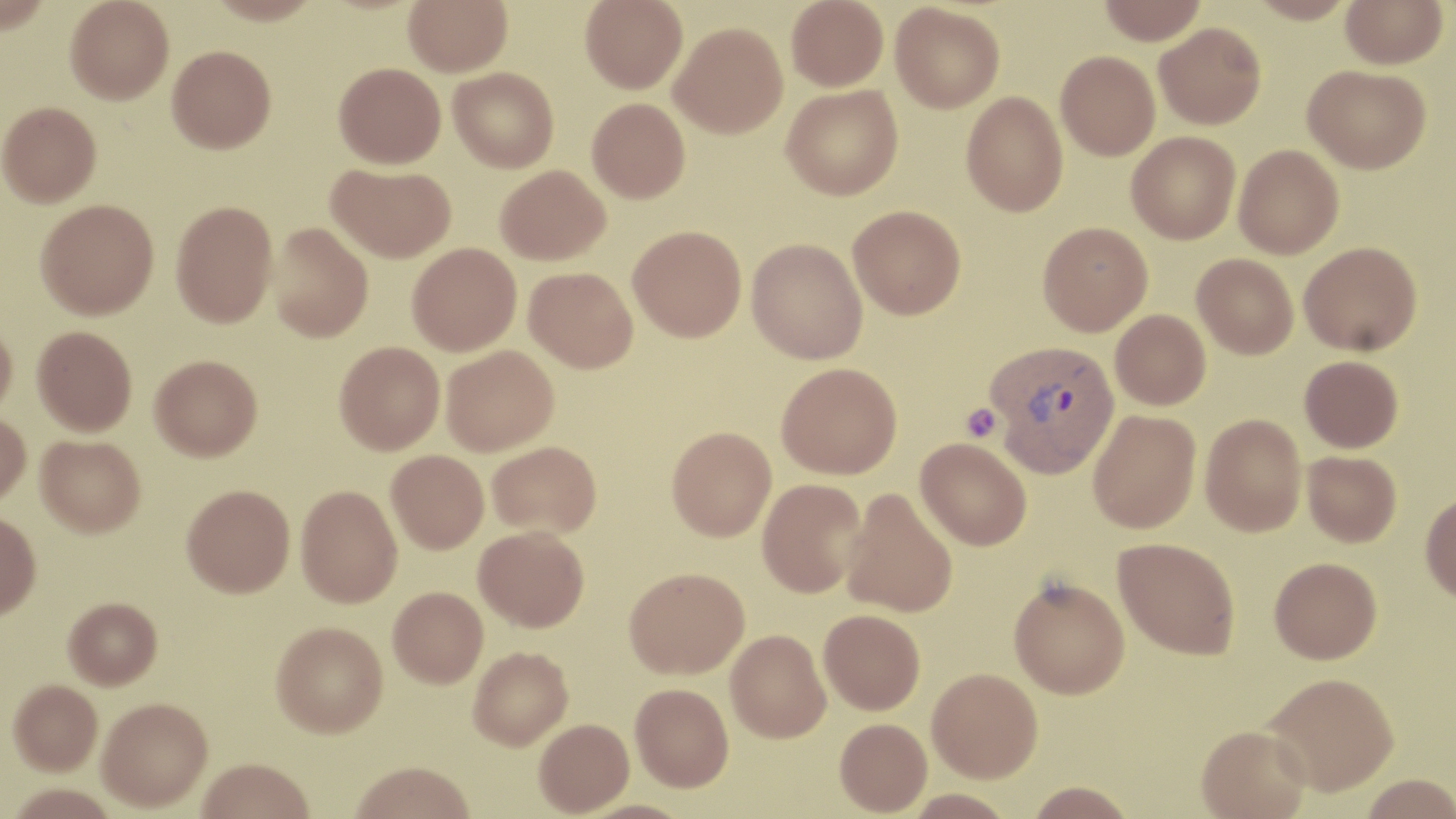
Summary:
  - Coordinate format: approximate bounding boxes as (x1, y1, x2, y2) in pixels
  - Uninfected red blood cell locations: (0, 0, 52, 34), (65, 0, 174, 104), (204, 0, 325, 25), (404, 0, 512, 76), (580, 0, 687, 93), (786, 0, 889, 90), (1096, 0, 1208, 43), (1245, 0, 1360, 23), (1341, 0, 1448, 68), (890, 3, 1005, 113), (669, 21, 788, 138), (1154, 22, 1266, 129), (167, 45, 276, 153), (1056, 51, 1160, 160), (333, 62, 446, 169), (1303, 64, 1431, 173), (449, 67, 558, 173), (781, 85, 902, 200), (961, 91, 1068, 217), (587, 98, 690, 203), (0, 101, 102, 207), (1127, 131, 1241, 244), (1233, 144, 1343, 258), (326, 162, 456, 262), (496, 165, 610, 265), (36, 198, 159, 319), (171, 200, 278, 327), (848, 204, 966, 319), (268, 222, 373, 342), (1037, 222, 1153, 335), (627, 225, 746, 341), (747, 238, 868, 364), (1299, 241, 1422, 355), (407, 243, 521, 355), (1192, 253, 1298, 359), (524, 266, 638, 372), (1110, 309, 1210, 410), (0, 320, 17, 421), (32, 325, 137, 436), (335, 341, 445, 454), (441, 345, 559, 456), (150, 354, 262, 461), (1300, 355, 1403, 452), (776, 362, 902, 479), (1088, 409, 1201, 533), (0, 410, 31, 507), (1200, 414, 1307, 536), (666, 426, 776, 541), (36, 434, 146, 537), (916, 437, 1032, 550), (487, 440, 601, 538), (386, 450, 489, 553), (1302, 451, 1402, 547), (757, 478, 868, 597), (182, 484, 295, 597), (296, 485, 402, 607), (841, 488, 958, 617), (1420, 492, 1456, 603), (0, 511, 41, 621), (474, 526, 589, 630), (1113, 537, 1240, 659), (1269, 557, 1381, 663), (624, 566, 749, 678), (1009, 576, 1130, 698), (388, 587, 488, 687), (63, 598, 162, 691), (819, 609, 925, 714), (271, 620, 388, 737), (726, 629, 831, 742), (468, 646, 573, 750), (927, 668, 1042, 782), (1265, 672, 1399, 795), (8, 682, 102, 778), (630, 682, 734, 791), (96, 700, 212, 814), (534, 718, 633, 816), (835, 718, 932, 816), (1197, 724, 1311, 819), (197, 760, 314, 819), (349, 761, 475, 819), (1359, 774, 1456, 819), (1026, 780, 1138, 818)
  - Plasmodium vivax-infected red blood cell locations: (985, 339, 1121, 477)
  - Platelet locations: (961, 403, 1002, 442)
  - Slide-level diagnosis: Plasmodium vivax
  - Magnification: 1000x
  - Modality: light microscopy
  - Field of view: single
  - Stain: May-Grünwald-Giemsa
  - Image size: 1456×819 pixels
  - Preparation: thin blood film